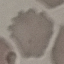

malaria_status: uninfected
image_type: cell patch, automatically extracted from a larger field of view and resized to 64 × 64 pixels
preparation: thin smear
capture: smartphone through the microscope eyepiece
stain: Giemsa